Assess this cell for malaria.
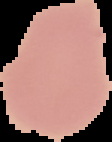

It is uninfected.

Image is 112×142 pixels. From a thin blood film. Cell region segmented out of the field of view; the surrounding area is masked to black.